Outline each Plasmodium falciparum-infected red blood cell.
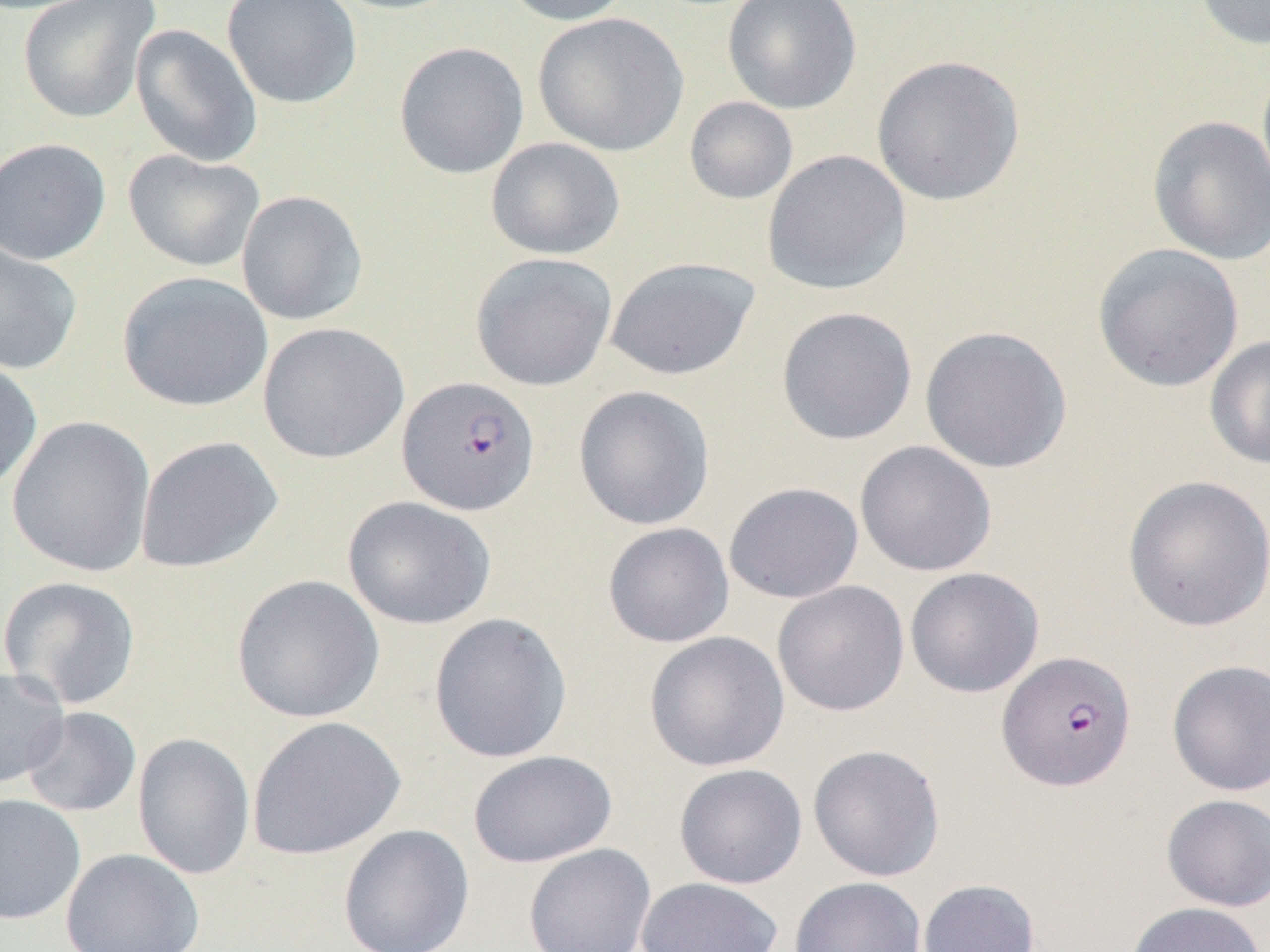
Approximate bounding boxes as [x1, y1, x2, y2] in pixels.
Plasmodium falciparum-infected red blood cells: [397, 376, 541, 515], [997, 651, 1137, 792].

Summary:
  - Uninfected red blood cell locations: [17, 0, 161, 123], [221, 0, 362, 109], [322, 0, 467, 15], [500, 0, 635, 26], [722, 0, 862, 114], [1192, 0, 1270, 51], [532, 12, 688, 156], [131, 24, 263, 167], [394, 41, 530, 179], [871, 55, 1026, 207], [1255, 60, 1270, 203], [684, 96, 799, 205], [1148, 114, 1270, 266], [0, 137, 111, 265], [485, 137, 625, 260], [123, 149, 265, 273], [762, 150, 911, 295], [236, 190, 369, 326], [0, 240, 83, 375], [1092, 243, 1245, 393], [470, 252, 618, 391], [605, 256, 761, 381], [117, 271, 274, 412], [776, 306, 918, 445], [258, 322, 409, 464], [919, 325, 1072, 474], [1204, 333, 1270, 470], [0, 357, 43, 493], [573, 385, 715, 530], [6, 415, 156, 578], [134, 435, 284, 574], [854, 440, 997, 577], [1122, 475, 1270, 632], [723, 482, 864, 603], [342, 496, 496, 630], [602, 522, 735, 648], [905, 567, 1044, 698], [231, 573, 385, 723], [0, 575, 143, 710], [772, 580, 910, 716], [428, 612, 573, 763], [644, 631, 791, 772], [1166, 659, 1270, 797], [0, 667, 70, 789], [21, 706, 141, 817], [246, 715, 406, 861], [133, 732, 256, 881], [808, 744, 945, 882], [467, 749, 618, 868], [673, 763, 808, 889], [0, 793, 87, 925], [1161, 793, 1270, 912], [338, 824, 475, 952], [523, 843, 657, 952], [61, 848, 205, 952], [789, 876, 926, 952], [635, 877, 785, 952], [917, 878, 1041, 952], [1123, 901, 1269, 952]
  - Slide-level diagnosis: Plasmodium falciparum
  - Field of view: one of a larger specimen
  - Preparation: thin blood film
  - Magnification: 1000x
  - Image size: 1270×952 pixels
  - Modality: optical microscopy